Evaluate for malaria.
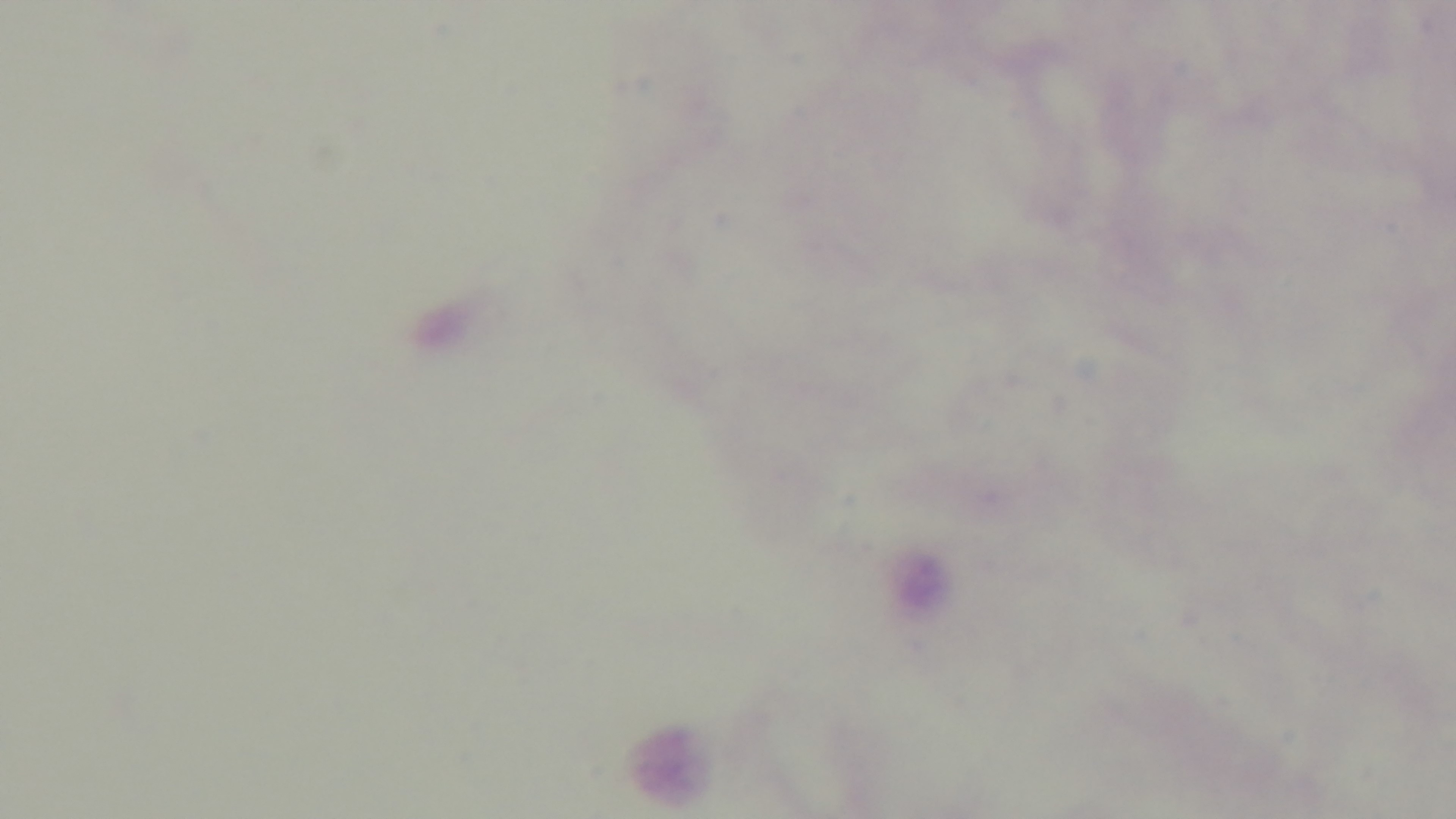

Negative.

modality = light microscopy
field of view = single
preparation = thick
objective = 100x oil immersion
capture = mounted 4K digital camera
stain = Giemsa